Comment on the morphology of the red blood cells.
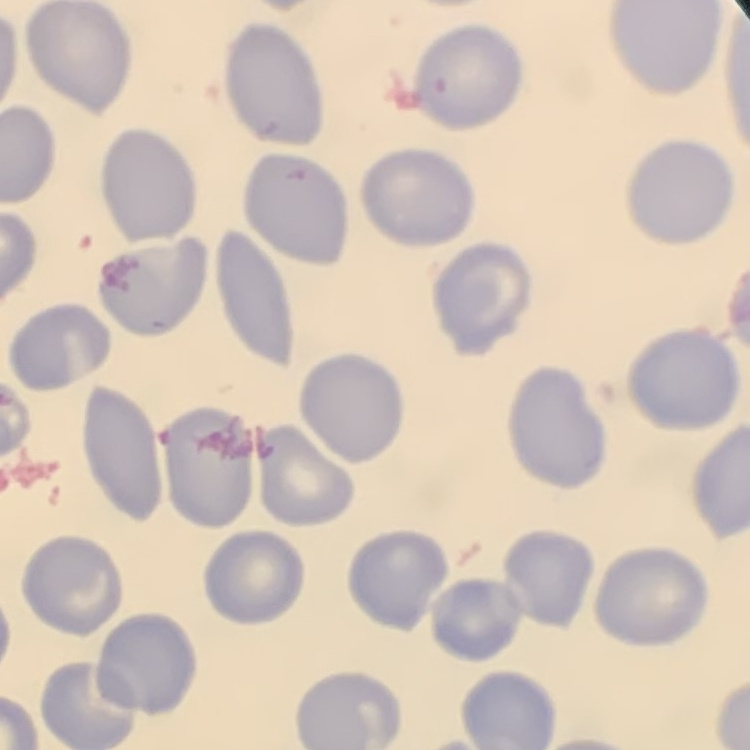
They show no rouleaux formation.

preparation = thin peripheral smear
image type = square crop of a larger photomicrograph
stain = Field's or Giemsa